Point out each Plasmodium parasite.
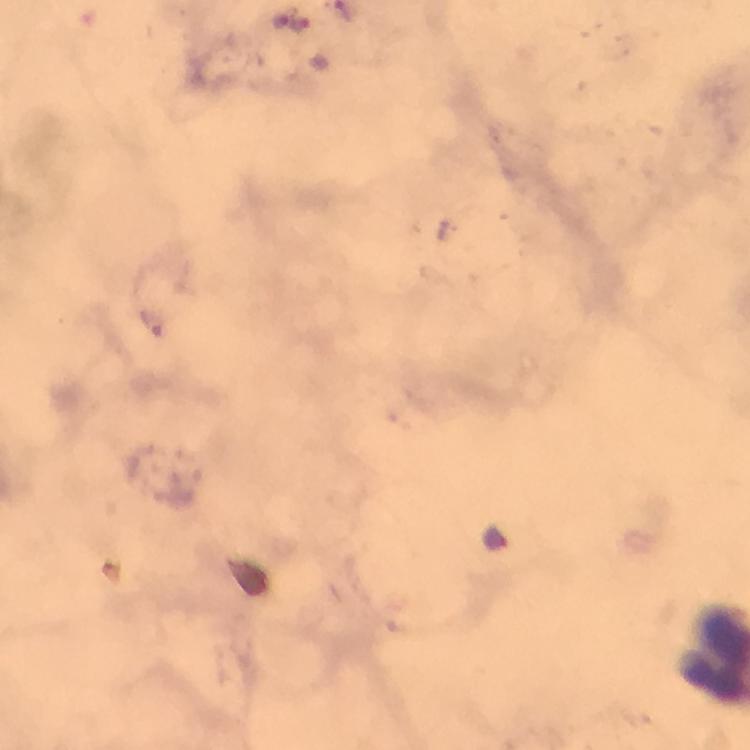
Approximate object centers, in pixels from the top-left corner.
Plasmodium parasites: (x=282, y=21), (x=301, y=23).

Photographed with a smartphone mounted on the microscope. Image is 750×750 pixels. From a diagnostic examination for malaria. Thick smear. A crop from one field of view. At 100x magnification. Immersion oil was used. Giemsa stain.